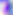
400x magnification. Toxoplasma gondii is shown. Micrograph.